Locate every parasitized RBC.
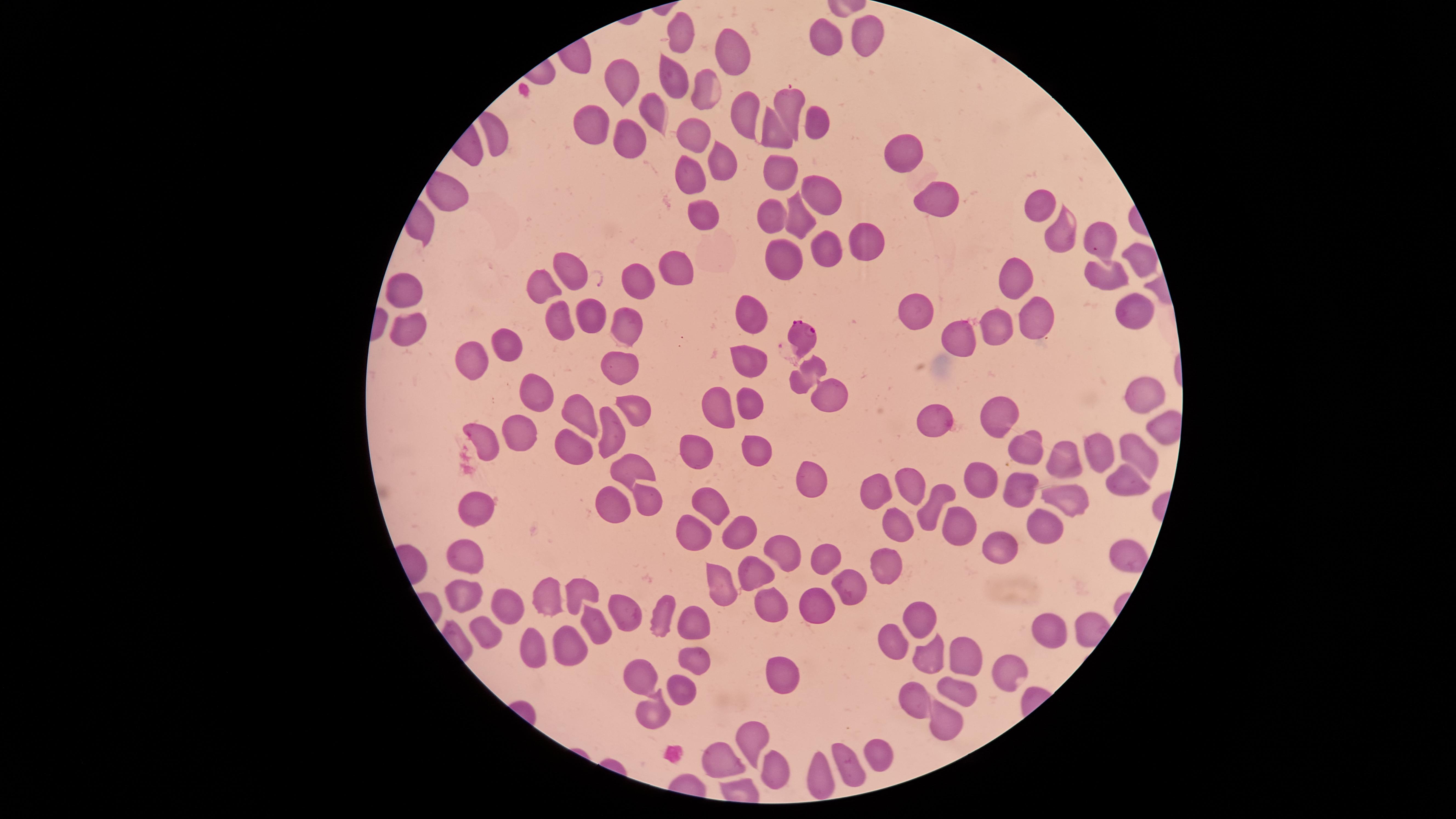

Approximate marker points, in pixels from the top-left corner.
Parasitized RBCs: (x=804, y=334), (x=829, y=394).

visible region = circular
species = Plasmodium falciparum
preparation = thin blood smear
field of view = single
uninfected RBCs = approximate marker points, in pixels from the top-left corner: (x=680, y=32), (x=867, y=37), (x=820, y=38), (x=733, y=48), (x=671, y=76), (x=617, y=79), (x=705, y=90), (x=790, y=107), (x=648, y=111), (x=748, y=114), (x=817, y=125), (x=588, y=128), (x=494, y=135), (x=770, y=135), (x=693, y=137), (x=629, y=139), (x=901, y=152), (x=720, y=159), (x=777, y=169), (x=693, y=173), (x=822, y=188), (x=935, y=197), (x=1037, y=206), (x=704, y=209), (x=775, y=213), (x=799, y=214), (x=1062, y=232), (x=1098, y=235), (x=866, y=242), (x=826, y=246), (x=789, y=253), (x=1140, y=256), (x=679, y=266), (x=566, y=271), (x=1106, y=274), (x=1015, y=280), (x=637, y=281), (x=402, y=287), (x=544, y=287), (x=1133, y=309), (x=749, y=312), (x=918, y=312), (x=1029, y=315), (x=591, y=319), (x=559, y=322), (x=628, y=327), (x=1001, y=327), (x=408, y=328), (x=958, y=334), (x=501, y=343), (x=749, y=356), (x=474, y=362), (x=617, y=367), (x=531, y=389), (x=1137, y=395), (x=710, y=400), (x=747, y=402), (x=640, y=407), (x=579, y=410), (x=1002, y=411), (x=932, y=418), (x=610, y=426), (x=519, y=430), (x=483, y=433), (x=571, y=442), (x=1030, y=447), (x=751, y=449), (x=1135, y=449), (x=1100, y=451), (x=692, y=452), (x=1056, y=456), (x=633, y=469), (x=1118, y=477), (x=813, y=480), (x=976, y=480), (x=1010, y=483), (x=876, y=486), (x=914, y=487), (x=647, y=496), (x=1065, y=503), (x=935, y=505), (x=710, y=506), (x=475, y=507), (x=605, y=507), (x=956, y=520), (x=1039, y=522), (x=693, y=526), (x=893, y=526), (x=738, y=532), (x=1000, y=548), (x=780, y=549), (x=464, y=551), (x=1122, y=551), (x=826, y=558), (x=883, y=565), (x=718, y=579), (x=759, y=579), (x=850, y=583), (x=580, y=590), (x=462, y=595), (x=555, y=597), (x=504, y=599), (x=815, y=601), (x=773, y=606), (x=619, y=608), (x=921, y=611), (x=662, y=613), (x=696, y=622), (x=1047, y=626), (x=486, y=633), (x=599, y=633), (x=894, y=639), (x=566, y=648), (x=529, y=653), (x=932, y=655), (x=969, y=657), (x=694, y=660), (x=1008, y=668), (x=783, y=672), (x=637, y=674), (x=679, y=684), (x=955, y=685), (x=919, y=703), (x=653, y=719), (x=940, y=723), (x=750, y=737), (x=879, y=754), (x=719, y=757), (x=852, y=759), (x=773, y=765), (x=822, y=772)
stain = Giemsa
capture = smartphone photograph through the microscope eyepiece
image size = 1456×819 pixels